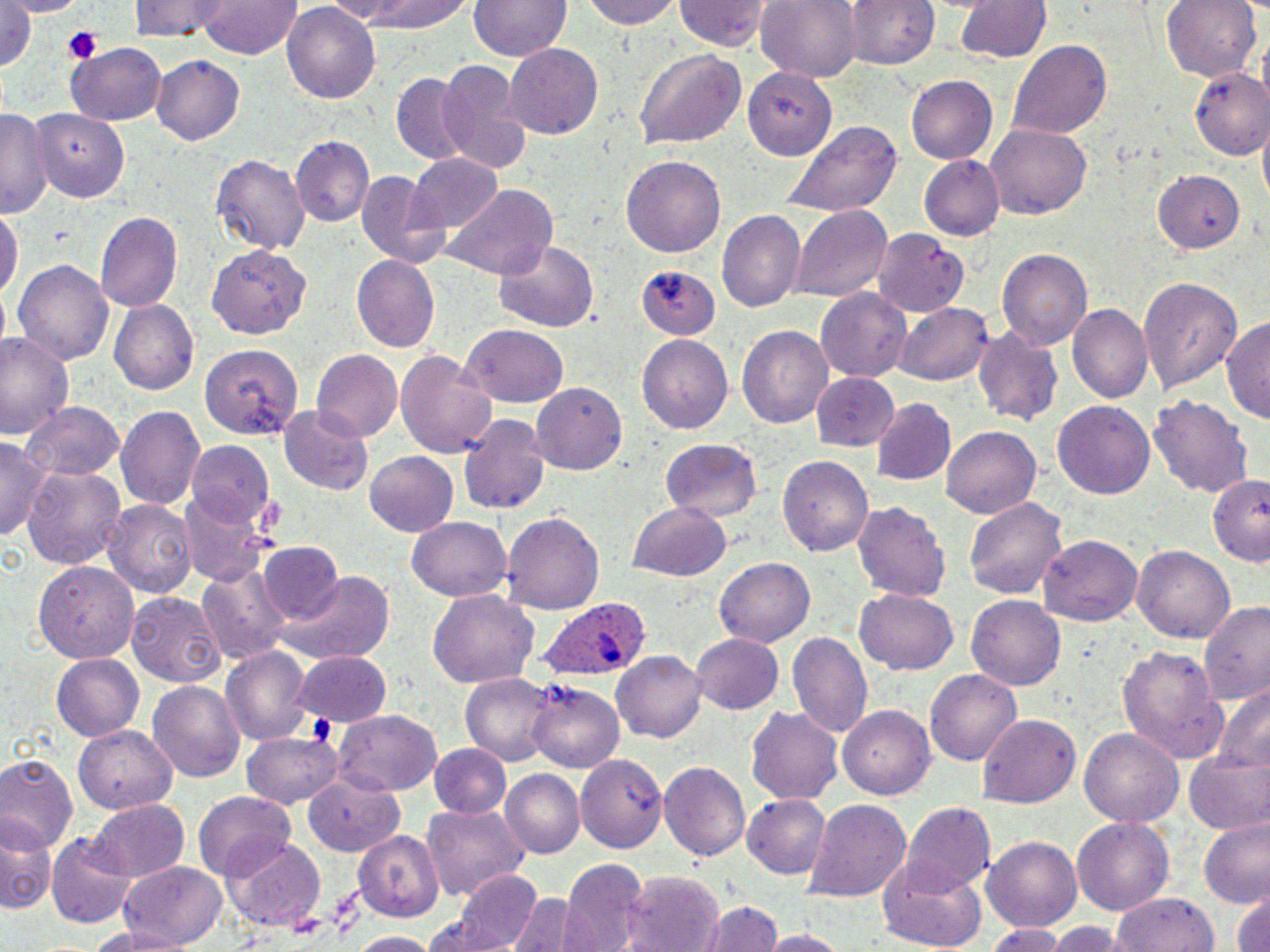
slide_level_diagnosis: Plasmodium ovale
modality: optical microscopy
magnification: 1000x
platelet_locations: 'approximate bounding boxes as (x1, y1, x2, y2) in pixels: (64, 31, 102, 63)'
field_of_view: one of a larger specimen
preparation: thin blood smear
stain: May-Grünwald-Giemsa
uninfected_red_blood_cell_locations: 'approximate bounding boxes as (x1, y1, x2, y2) in pixels: (8, 0, 78, 15), (130, 0, 233, 41), (197, 0, 304, 61), (331, 0, 473, 32), (471, 0, 570, 63), (581, 0, 684, 30), (674, 0, 771, 51), (757, 0, 861, 80), (841, 0, 940, 71), (1161, 0, 1262, 83), (954, 1, 1050, 64), (1, 2, 38, 78), (283, 3, 383, 105), (1008, 40, 1110, 140), (67, 43, 166, 124), (502, 43, 602, 141), (634, 47, 747, 149), (152, 54, 245, 145), (436, 58, 532, 173), (746, 67, 837, 162), (1185, 67, 1270, 159), (391, 72, 471, 162), (905, 74, 1000, 164), (33, 107, 132, 203), (0, 108, 48, 217), (781, 121, 900, 216), (986, 124, 1091, 220), (293, 137, 373, 228), (209, 152, 311, 256), (409, 152, 504, 230), (620, 153, 725, 255), (918, 155, 1003, 241), (1155, 168, 1246, 254), (353, 171, 451, 271), (444, 186, 557, 281), (791, 205, 894, 303), (0, 207, 21, 305), (718, 210, 807, 315), (95, 212, 181, 313), (872, 229, 968, 317), (493, 239, 599, 333), (208, 243, 312, 340), (997, 250, 1092, 350), (351, 255, 439, 351), (12, 258, 114, 366), (637, 267, 717, 343), (1140, 277, 1243, 393), (815, 290, 910, 380), (107, 299, 198, 395), (897, 302, 992, 387), (1066, 305, 1151, 404), (1222, 315, 1270, 425), (459, 324, 571, 405), (737, 325, 833, 431), (972, 326, 1064, 429), (0, 328, 74, 439), (638, 336, 733, 434), (200, 345, 304, 439), (393, 348, 497, 459), (310, 350, 402, 441), (809, 371, 900, 450), (530, 382, 627, 473), (1149, 392, 1251, 497), (871, 398, 957, 486), (21, 400, 123, 482), (1053, 401, 1155, 500), (116, 404, 205, 509), (278, 404, 373, 496), (457, 414, 549, 518), (942, 426, 1040, 520), (0, 436, 51, 543), (659, 437, 762, 522), (189, 442, 273, 524), (364, 452, 458, 537), (776, 454, 875, 557), (22, 463, 126, 573), (1208, 474, 1269, 563), (181, 486, 277, 588), (963, 495, 1069, 600), (854, 499, 949, 604), (105, 500, 196, 600), (627, 502, 732, 582), (502, 509, 605, 615), (409, 515, 514, 602), (1040, 535, 1143, 624), (257, 544, 344, 627), (1134, 545, 1235, 642), (713, 555, 815, 648), (36, 557, 137, 684), (199, 563, 293, 664), (272, 571, 394, 663), (855, 589, 960, 674), (428, 590, 539, 688), (127, 592, 225, 686), (968, 595, 1069, 690), (1203, 600, 1270, 708), (789, 630, 872, 738), (691, 632, 785, 714), (1115, 644, 1229, 764), (221, 647, 312, 746), (613, 649, 705, 741), (291, 650, 392, 727), (51, 654, 144, 743), (925, 668, 1022, 765), (460, 673, 557, 765), (148, 679, 246, 782), (528, 681, 624, 774), (1212, 685, 1270, 776), (745, 703, 844, 805), (837, 704, 934, 800), (333, 710, 443, 796), (977, 714, 1081, 807), (78, 725, 176, 815), (1081, 727, 1183, 824), (243, 735, 344, 809), (0, 741, 140, 840), (430, 745, 511, 818), (1184, 749, 1270, 835), (573, 751, 666, 880), (0, 757, 78, 854), (658, 761, 750, 861), (501, 769, 583, 857), (304, 777, 404, 854), (194, 792, 295, 879), (742, 794, 831, 879), (805, 798, 911, 902), (85, 800, 188, 881), (899, 803, 995, 895), (421, 804, 529, 898), (1200, 816, 1270, 905), (1071, 817, 1174, 917), (2, 819, 51, 918), (353, 830, 445, 921), (47, 834, 135, 928), (984, 835, 1084, 932), (223, 839, 328, 932), (876, 857, 988, 950), (559, 859, 650, 952), (117, 864, 227, 947), (449, 868, 548, 952), (621, 872, 723, 952), (1231, 889, 1270, 952), (506, 892, 581, 952), (1111, 892, 1221, 952), (696, 902, 787, 951), (1048, 923, 1121, 952), (79, 924, 195, 952), (987, 924, 1067, 952), (755, 930, 853, 951), (354, 933, 436, 952)'
image_size: 1270×952 pixels
plasmodium_ovale_infected_red_blood_cell_locations: 'approximate bounding boxes as (x1, y1, x2, y2) in pixels: (540, 599, 650, 685)'